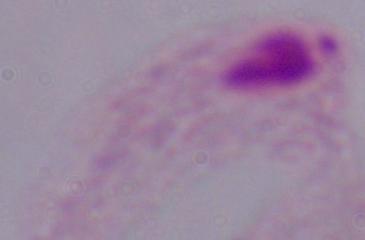
Summary:
  - Modality: micrograph
  - Identification: trichomonad
  - Magnification: 1000x